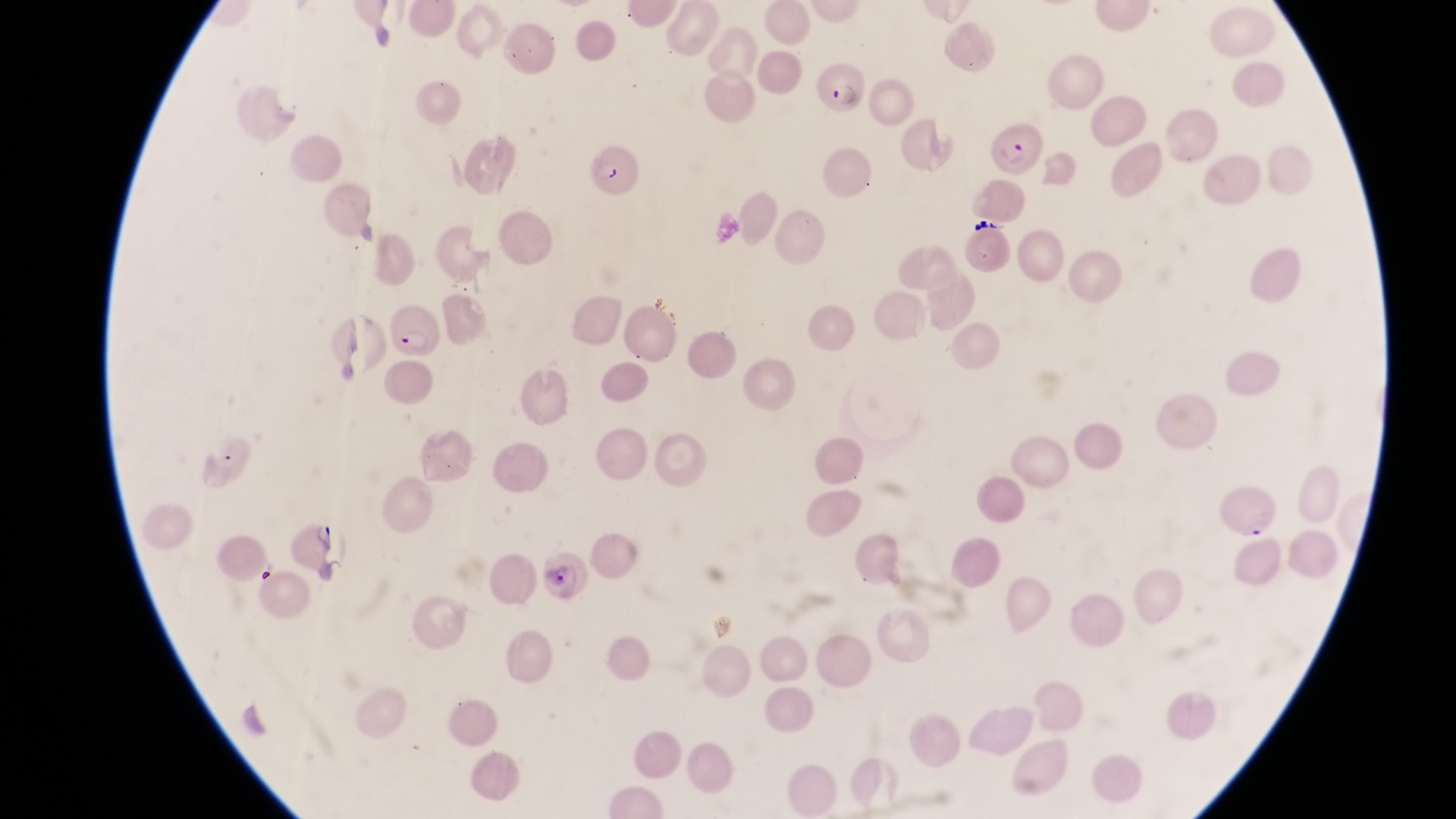 Approximate bounding boxes as {left, top, right, bottom} in pixels. Parasitised red blood cell locations: {812, 55, 865, 113}, {984, 118, 1043, 181}, {573, 122, 646, 202}, {383, 304, 446, 362}, {1215, 481, 1281, 542}, {285, 515, 344, 578}. Artifact (platelet-like body, stain precipitate, or debris) locations: {249, 558, 279, 590}. Captured by a smartphone held over the eyepiece of an Olympus CX-23 microscope. Magnification of 1000x. Thin blood smear. Image is 1456×819 pixels. Collected in Uganda. One field of view.